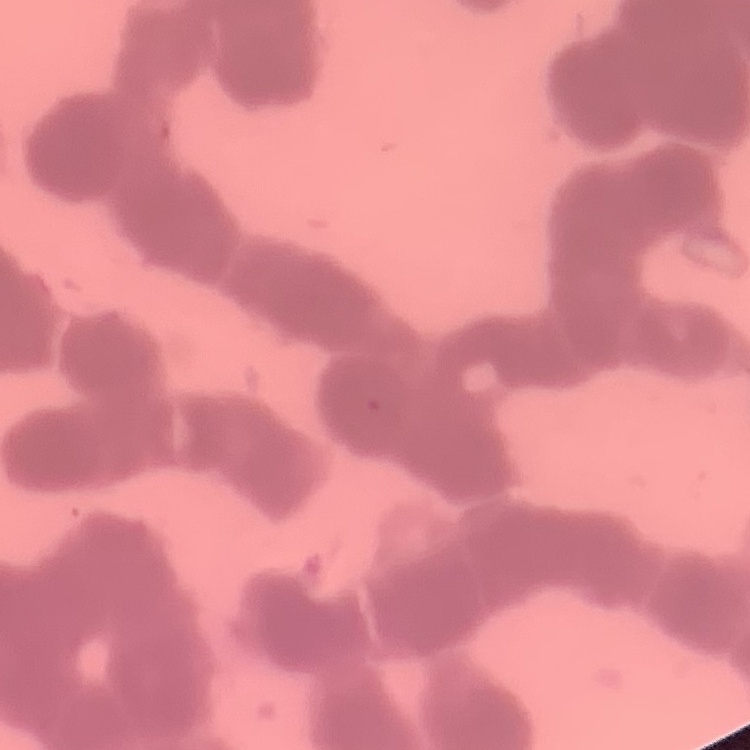
Summary:
  - Erythrocyte morphology: rouleaux formation
  - Preparation: thin blood film
  - Stain: Field's or Giemsa
  - Image type: square crop of a larger photomicrograph